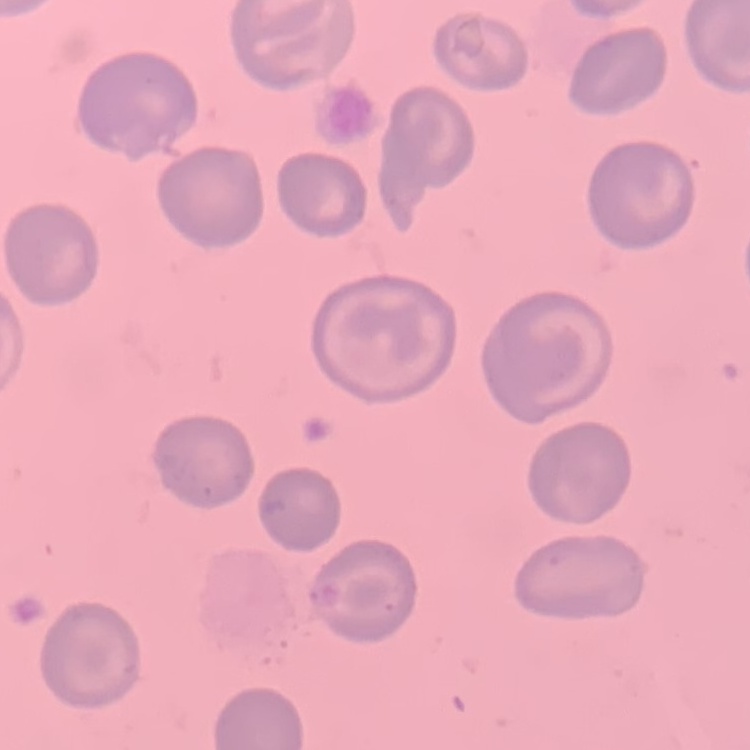
Summary:
  - Red blood cell morphology: no rouleaux formation
  - Stain: Field's or Giemsa
  - Image type: one tile cut from a larger photomicrograph
  - Preparation: thin blood film